Locate and identify every blood parasite.
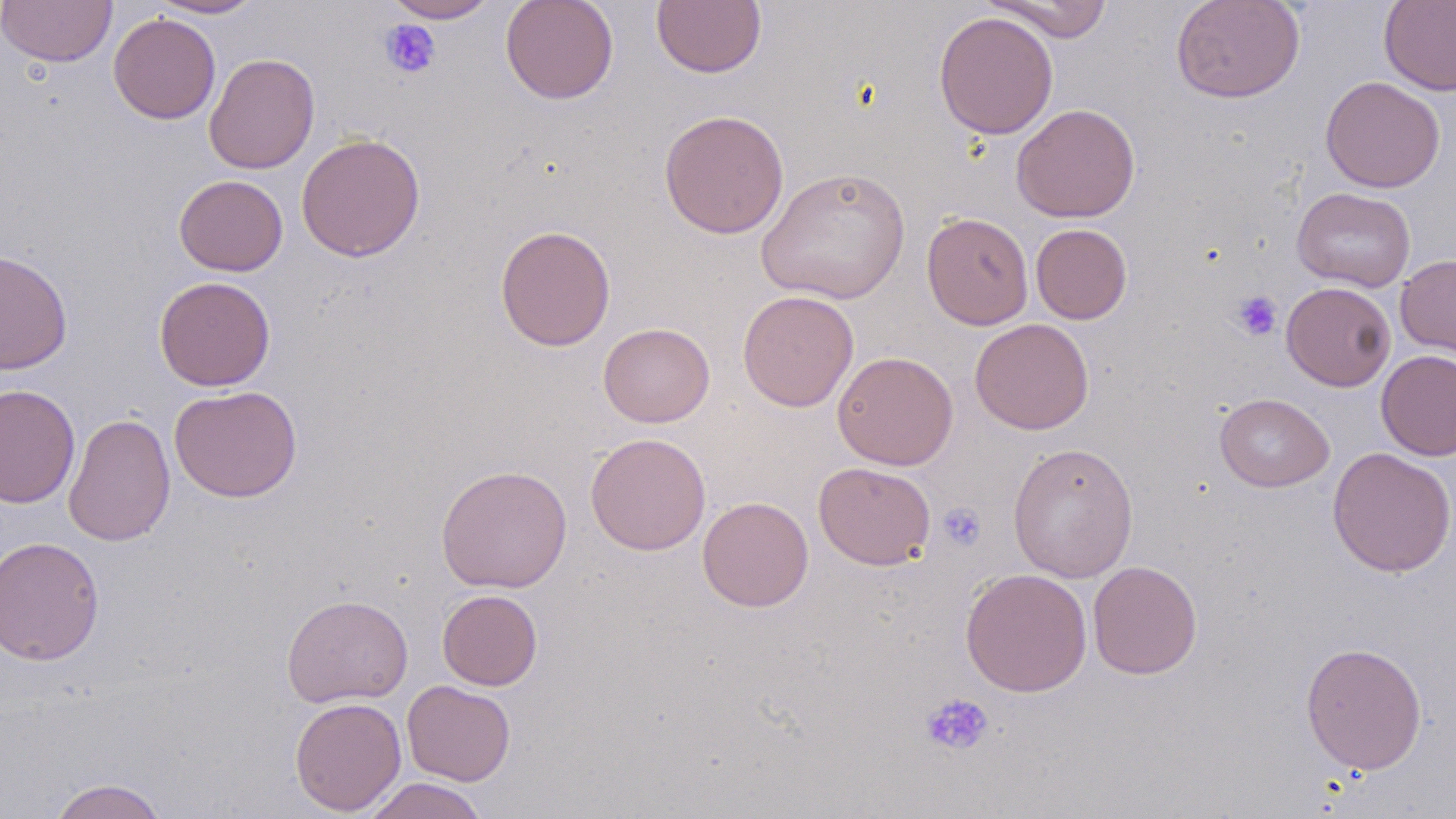
No blood parasites observed.

Approximate bounding boxes as (x1, y1, x2, y2) in pixels. Uninfected red blood cell locations: (0, 0, 118, 67), (148, 0, 264, 19), (382, 0, 500, 22), (500, 0, 619, 104), (651, 0, 767, 77), (1171, 0, 1306, 103), (982, 1, 1114, 42), (1378, 1, 1456, 96), (933, 11, 1059, 139), (108, 12, 221, 124), (204, 52, 321, 175), (1320, 76, 1445, 193), (1011, 103, 1141, 223), (658, 109, 789, 239), (296, 133, 425, 261), (757, 166, 911, 305), (174, 175, 288, 276), (1292, 187, 1416, 292), (921, 212, 1033, 330), (1031, 223, 1132, 324), (495, 224, 616, 351), (0, 249, 73, 375), (1395, 254, 1456, 358), (154, 276, 276, 391), (1281, 281, 1396, 391), (737, 290, 859, 413), (970, 318, 1094, 435), (598, 322, 715, 427), (1376, 349, 1456, 461), (832, 351, 959, 470), (0, 384, 80, 509), (169, 385, 302, 503), (1215, 393, 1334, 492), (63, 412, 176, 547), (585, 432, 711, 555), (1007, 442, 1139, 583), (1327, 447, 1456, 577), (813, 462, 936, 570), (435, 464, 573, 593), (697, 496, 814, 612), (0, 535, 104, 666), (1087, 560, 1203, 679), (960, 568, 1092, 696), (437, 589, 543, 691), (281, 594, 413, 707), (1300, 642, 1427, 774), (402, 680, 516, 785), (289, 696, 406, 815), (362, 777, 489, 819), (48, 778, 169, 819). Platelet locations: (379, 19, 442, 80), (1231, 290, 1282, 341), (937, 502, 986, 552), (920, 692, 995, 756). Slide-level diagnosis: negative for blood parasites. Captured at 1000x magnification. Light microscopy. Image is 1456×819 pixels. Thin blood smear. May-Grünwald-Giemsa stain. One field of a larger specimen.